Classify this cell by malaria status.
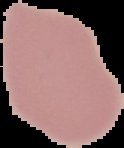

It is uninfected.

image size = 124×148 pixels
preparation = thin blood smear
image type = segmented cell region on a black background